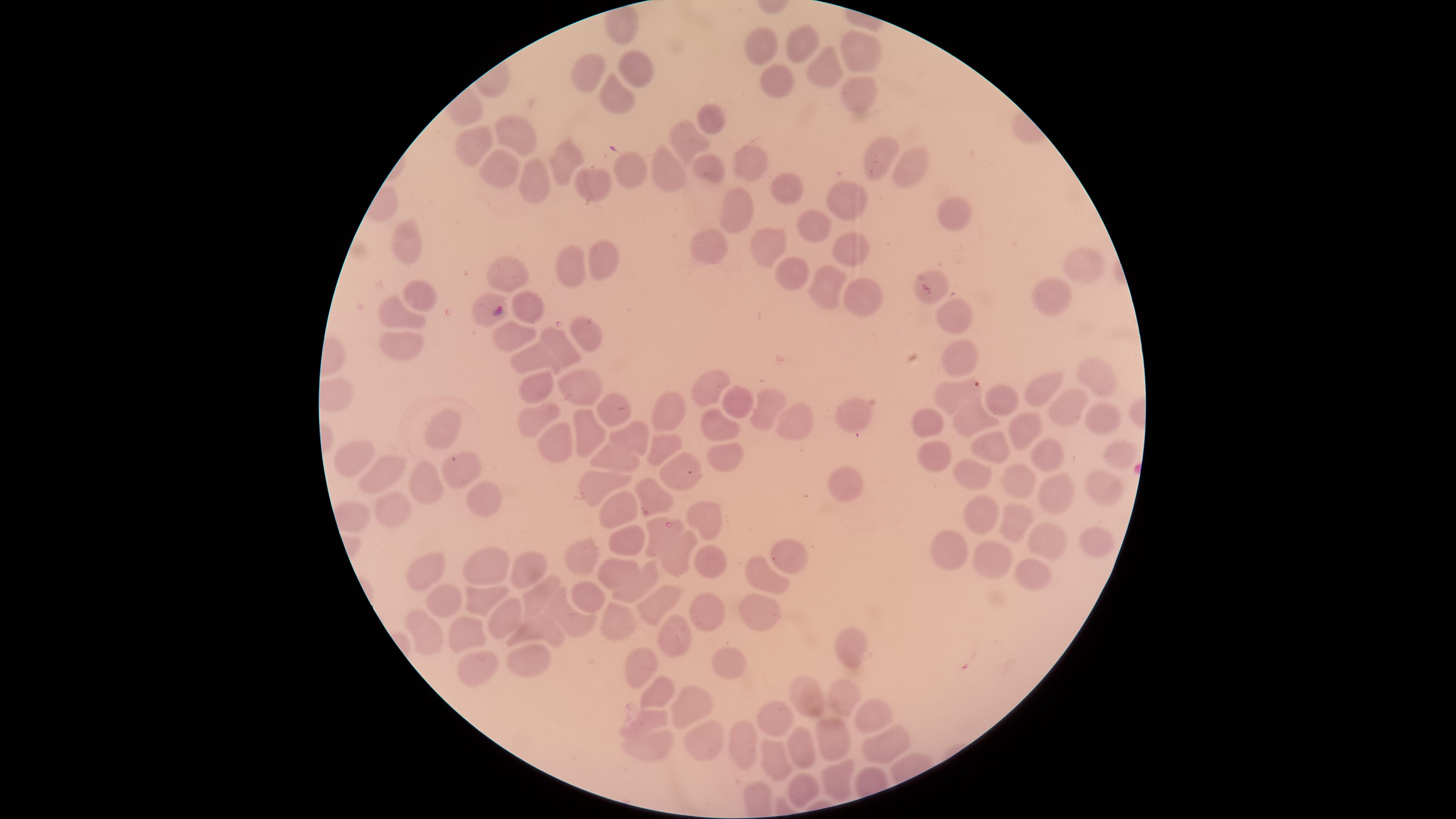

capture = smartphone photograph through the microscope eyepiece
visible region = circular
uninfected red blood cells = approximate marker points as {x, y} in pixels: {618, 31}, {805, 41}, {761, 47}, {863, 50}, {636, 67}, {828, 67}, {588, 74}, {781, 79}, {857, 92}, {618, 98}, {710, 121}, {516, 138}, {688, 140}, {469, 146}, {878, 152}, {564, 155}, {748, 159}, {504, 167}, {906, 169}, {632, 170}, {706, 173}, {667, 175}, {590, 177}, {537, 180}, {786, 181}, {846, 196}, {738, 208}, {956, 212}, {810, 223}, {769, 243}, {409, 246}, {850, 246}, {704, 249}, {599, 259}, {1079, 262}, {567, 269}, {788, 270}, {505, 278}, {824, 284}, {859, 291}, {934, 291}, {427, 292}, {1052, 294}, {528, 303}, {391, 310}, {958, 317}, {586, 330}, {399, 345}, {559, 347}, {964, 352}, {533, 360}, {1100, 370}, {709, 385}, {576, 388}, {1042, 390}, {960, 394}, {531, 397}, {1002, 401}, {738, 402}, {768, 403}, {614, 405}, {1066, 410}, {674, 411}, {851, 411}, {975, 415}, {1106, 415}, {528, 418}, {719, 419}, {795, 421}, {579, 426}, {929, 426}, {1025, 427}, {445, 430}, {626, 437}, {556, 440}, {659, 445}, {996, 450}, {1117, 452}, {613, 453}, {725, 453}, {933, 453}, {1050, 454}, {360, 457}, {458, 465}, {385, 468}, {681, 469}, {972, 473}, {424, 483}, {1020, 483}, {606, 485}, {845, 486}, {1102, 487}, {1058, 492}, {484, 498}, {653, 498}, {391, 504}, {980, 509}, {615, 516}, {705, 519}, {1015, 522}, {626, 539}, {1093, 540}, {1044, 541}, {951, 547}, {583, 554}, {677, 557}, {786, 557}, {993, 563}, {479, 565}, {709, 566}, {428, 569}, {619, 569}, {521, 570}, {1028, 575}, {765, 578}, {635, 588}, {531, 596}, {446, 600}, {586, 600}, {482, 601}, {652, 604}, {750, 607}, {568, 616}, {700, 616}, {507, 621}, {615, 622}, {546, 624}, {428, 627}, {464, 630}, {675, 636}, {844, 644}, {527, 657}, {734, 661}, {643, 667}, {471, 669}, {803, 693}, {845, 693}, {660, 698}, {684, 704}, {771, 711}, {866, 717}, {645, 720}, {828, 738}, {698, 742}, {743, 746}, {885, 748}, {651, 749}, {796, 755}, {772, 759}, {842, 772}, {799, 791}
presence = malaria parasites identified
species = Plasmodium falciparum
parasitized red blood cells = approximate marker points as {x, y} in pixels: {492, 310}, {668, 525}
image size = 1456×819 pixels
stain = Giemsa
preparation = thin blood film
field of view = single